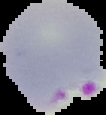

result = Plasmodium parasites identified
image size = 106×115 pixels
image type = segmented cell region on a black background
preparation = thin blood smear